Identify the parasite.
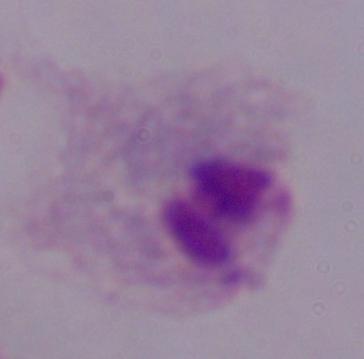

This is a trichomonad.

Summary:
  - Modality: micrograph
  - Magnification: 1000x